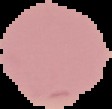

Summary:
  - Preparation: thin blood film
  - Image type: segmented cell region on a black background
  - Image size: 112×109 pixels
  - Result: no Plasmodium parasites detected